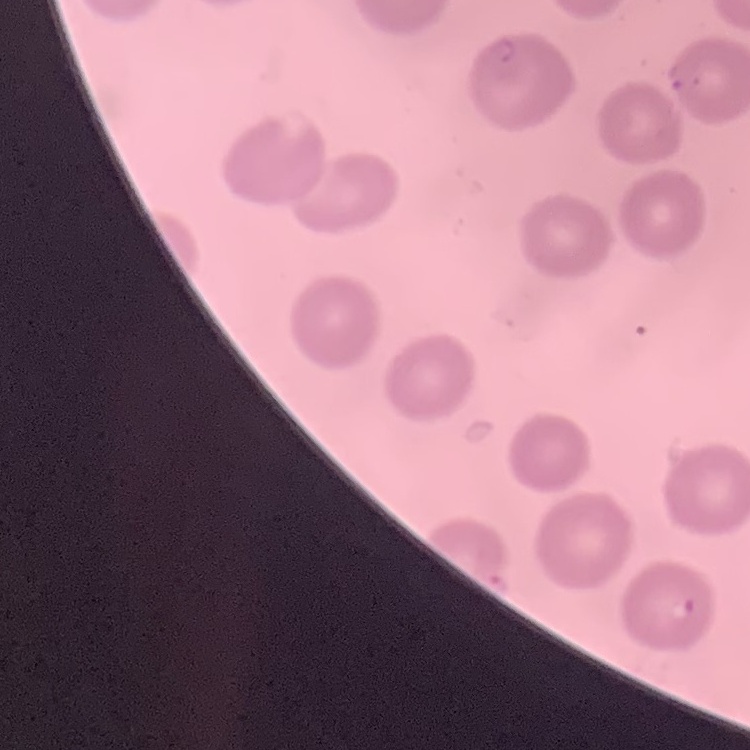

Summary:
  - Red blood cell morphology: no rouleaux formation
  - Stain: Field's or Giemsa
  - Preparation: thin blood film
  - Image type: square crop of a larger photomicrograph